State which parasite is depicted.
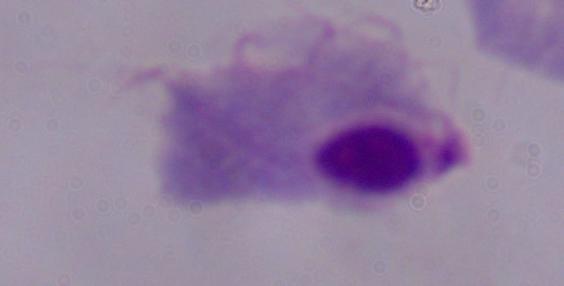
A trichomonad.

{
  "modality": "micrograph",
  "magnification": "1000x"
}